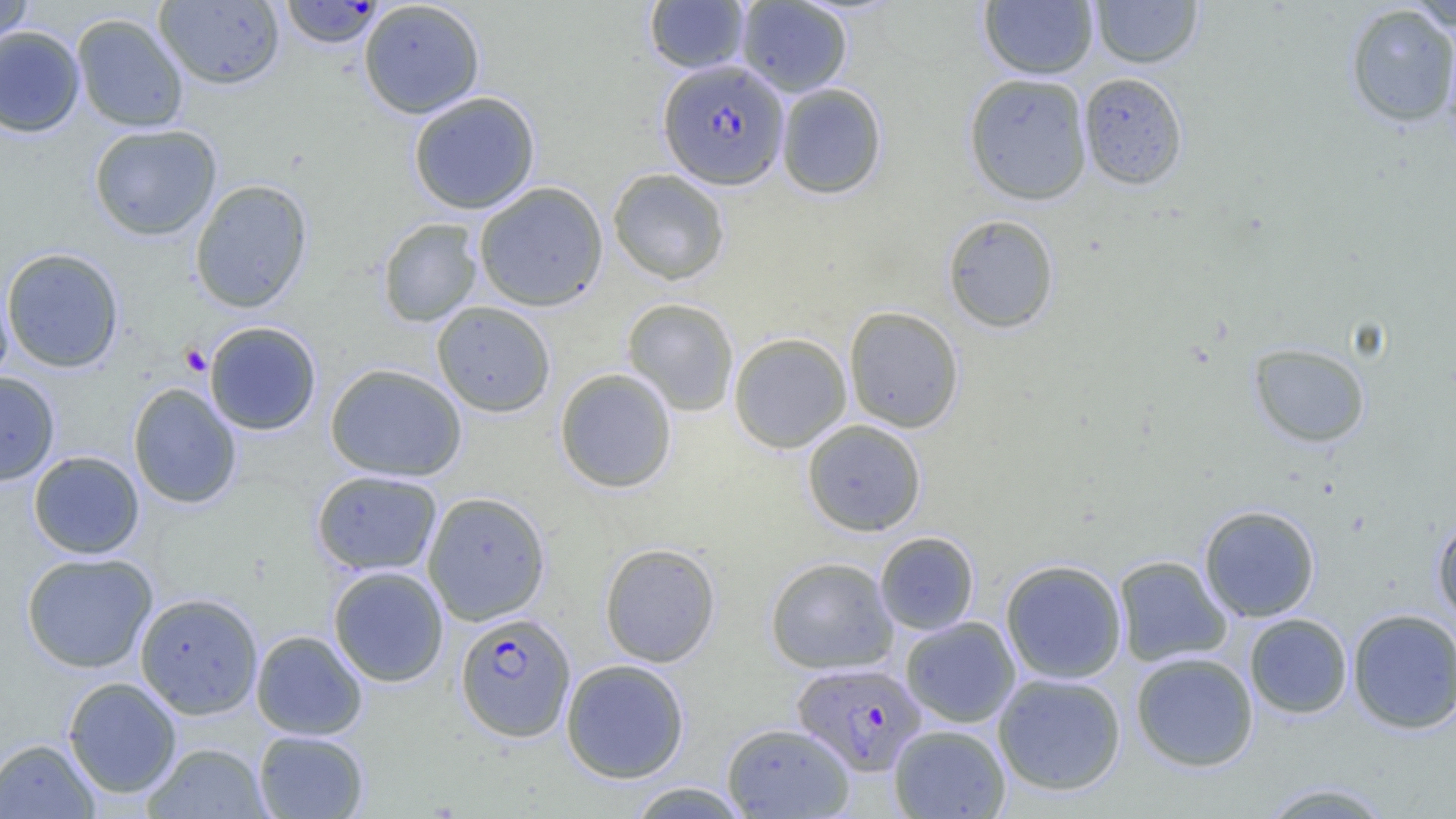 Approximate bounding boxes as [x1, y1, x2, y2] in pixels. Plasmodium falciparum-infected red blood cell locations: [280, 1, 384, 49], [658, 60, 790, 190], [455, 611, 576, 742], [792, 662, 926, 775]. Uninfected red blood cell locations: [0, 0, 34, 49], [358, 0, 485, 119], [644, 0, 750, 74], [736, 0, 852, 97], [978, 0, 1099, 80], [1090, 0, 1203, 68], [154, 1, 285, 89], [1406, 2, 1456, 33], [1345, 4, 1456, 127], [71, 14, 189, 133], [1441, 21, 1456, 154], [0, 26, 84, 138], [1078, 72, 1189, 190], [963, 73, 1093, 205], [776, 82, 887, 199], [408, 91, 541, 215], [88, 123, 222, 241], [608, 169, 730, 285], [189, 179, 313, 313], [473, 182, 609, 312], [942, 214, 1060, 333], [377, 218, 482, 327], [1, 248, 124, 373], [0, 271, 14, 388], [622, 298, 739, 416], [431, 301, 556, 417], [843, 305, 965, 434], [204, 321, 321, 436], [728, 332, 852, 453], [1249, 342, 1371, 448], [325, 363, 467, 482], [554, 368, 677, 493], [0, 372, 60, 485], [128, 382, 242, 509], [801, 419, 927, 536], [28, 451, 144, 559], [311, 470, 443, 576], [422, 491, 551, 625], [1198, 504, 1321, 622], [1431, 515, 1456, 626], [874, 531, 979, 636], [599, 542, 721, 668], [21, 552, 158, 673], [1113, 555, 1232, 666], [764, 556, 899, 675], [1000, 559, 1127, 684], [328, 566, 449, 687], [135, 591, 263, 720], [1347, 607, 1456, 734], [1244, 613, 1353, 719], [900, 616, 1021, 728], [251, 630, 367, 740], [1130, 651, 1259, 772], [560, 659, 690, 783], [992, 672, 1127, 796], [63, 677, 182, 798], [721, 722, 855, 818], [888, 724, 1011, 818], [253, 730, 370, 818], [0, 738, 100, 818], [142, 742, 270, 818], [624, 781, 754, 819], [1256, 781, 1399, 818]. Platelet locations: [179, 343, 211, 376]. Slide-level diagnosis: Plasmodium falciparum. Thin blood film. Light microscopy. Captured at 1000x magnification. One field of a larger specimen. Image is 1456×819 pixels.